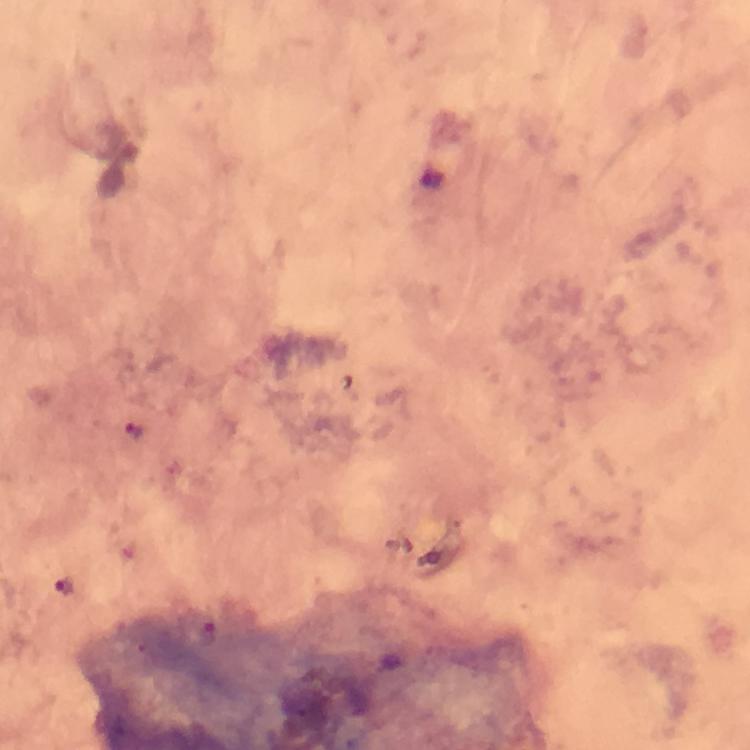
{
  "cropped_from": "one field of view",
  "preparation": "thick smear",
  "malaria_parasite_locations": "approximate object centers, in pixels from the top-left corner: (x=131, y=430), (x=62, y=585)",
  "magnification": "100x",
  "capture": "smartphone photograph through a microscope",
  "image_size": "750×750 pixels",
  "stain": "Giemsa",
  "context": "from a diagnostic examination for malaria",
  "immersion_oil": "applied"
}